Assess the morphology of the red blood cells.
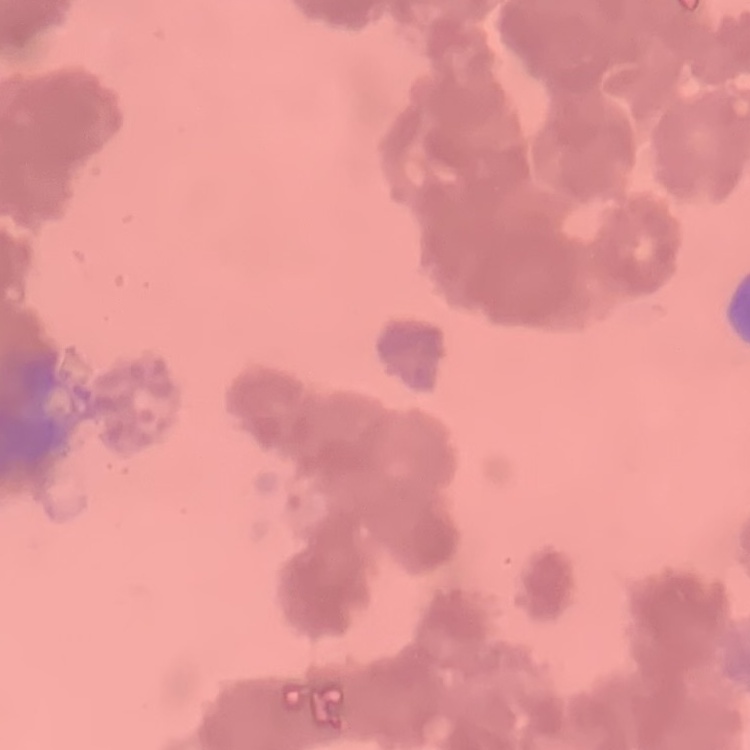

Rouleaux formation.

preparation: thin peripheral smear
image_type: one tile cut from a larger photomicrograph
stain: Field's or Giemsa